Assess this cell for malaria.
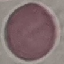

Uninfected.

Acquired by smartphone through the microscope eyepiece. Giemsa stain. Thin smear of blood. Automatically extracted cell patch, resized to 64 × 64 pixels.